Locate every blood parasite and identify its species.
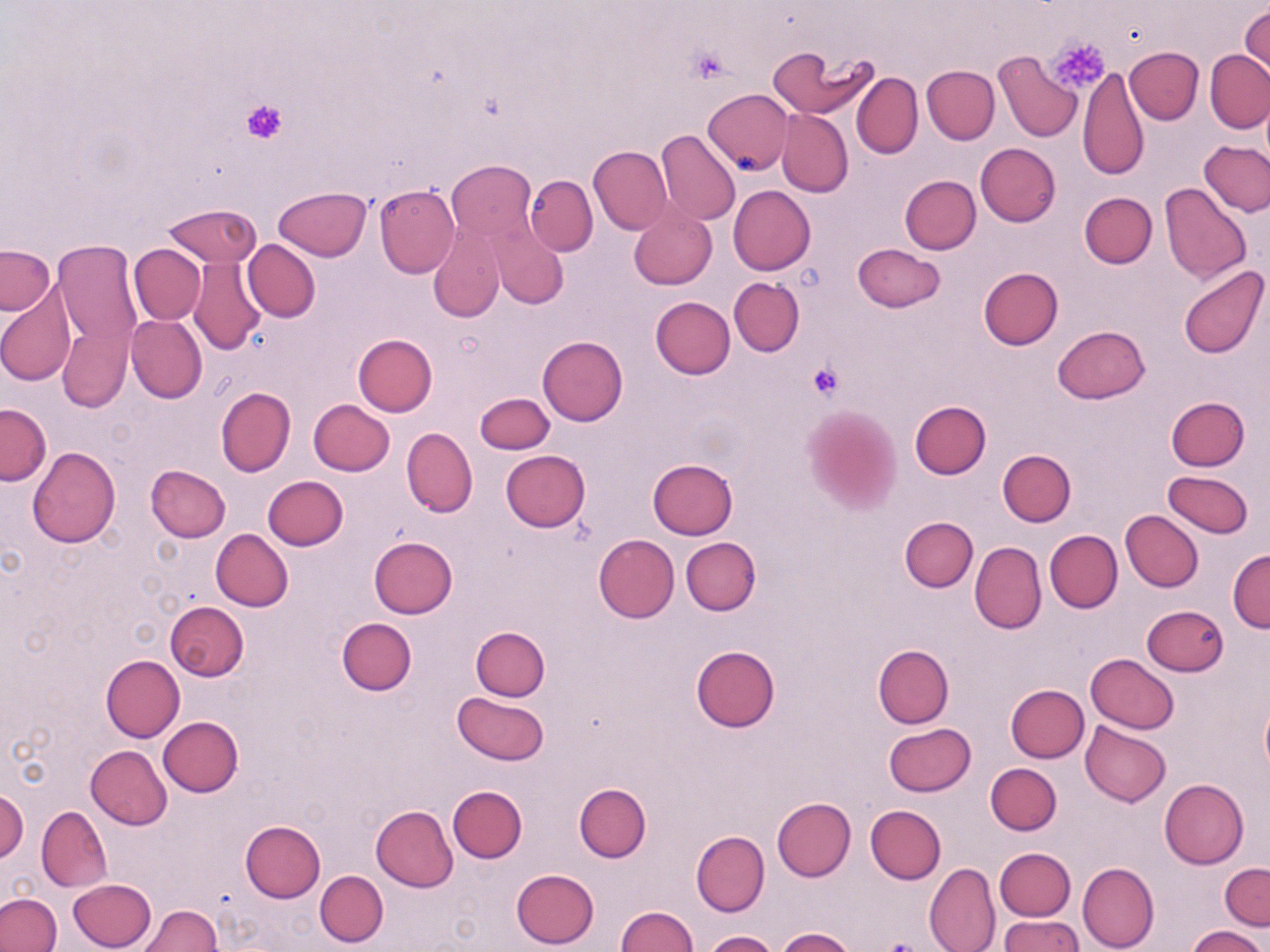

No blood parasites observed.

Approximate bounding boxes as (x1, y1, x2, y2) in pixels. Platelet locations: (1046, 37, 1110, 94), (688, 46, 733, 82), (242, 99, 288, 144), (807, 361, 846, 400), (878, 940, 928, 952). Uninfected red blood cell locations: (1240, 4, 1269, 82), (768, 43, 878, 121), (1125, 47, 1203, 123), (1206, 50, 1270, 134), (994, 51, 1082, 142), (922, 65, 1000, 144), (1078, 67, 1149, 181), (851, 73, 923, 158), (703, 88, 793, 174), (777, 109, 853, 196), (655, 128, 741, 226), (1199, 141, 1270, 215), (976, 143, 1061, 226), (588, 146, 671, 234), (447, 161, 536, 239), (526, 175, 598, 256), (900, 175, 981, 254), (1160, 183, 1251, 285), (374, 184, 459, 278), (274, 185, 372, 260), (728, 186, 815, 274), (1080, 192, 1157, 268), (628, 201, 717, 290), (164, 203, 260, 268), (488, 223, 566, 309), (428, 224, 505, 322), (54, 239, 142, 379), (242, 240, 320, 322), (129, 244, 206, 324), (852, 244, 945, 312), (1, 245, 54, 315), (189, 257, 268, 354), (1177, 264, 1268, 360), (978, 267, 1062, 350), (729, 277, 804, 355), (0, 285, 78, 387), (651, 296, 735, 378), (126, 315, 207, 403), (58, 324, 132, 413), (1051, 325, 1149, 404), (352, 334, 437, 417), (538, 336, 628, 426), (216, 387, 296, 476), (475, 392, 554, 454), (1166, 397, 1249, 471), (309, 399, 395, 476), (909, 401, 990, 479), (0, 403, 50, 484), (801, 407, 900, 513), (401, 429, 477, 517), (26, 447, 120, 547), (997, 449, 1076, 526), (501, 450, 590, 531), (647, 459, 738, 540), (146, 465, 230, 541), (1162, 469, 1254, 538), (263, 476, 348, 550), (1121, 510, 1204, 591), (900, 516, 978, 593), (211, 528, 293, 611), (1045, 530, 1122, 612), (594, 534, 680, 622), (368, 536, 458, 618), (681, 537, 760, 616), (970, 541, 1047, 636), (1228, 549, 1270, 633), (164, 601, 249, 681), (1141, 604, 1230, 677), (336, 619, 416, 695), (471, 626, 551, 700), (873, 644, 953, 728), (690, 646, 779, 732), (1084, 653, 1180, 733), (101, 655, 185, 741), (1005, 685, 1088, 762), (452, 692, 549, 765), (1260, 698, 1270, 777), (158, 717, 243, 797), (1081, 720, 1171, 806), (884, 722, 976, 795), (86, 746, 173, 829), (986, 762, 1061, 835), (1159, 778, 1248, 867), (575, 782, 651, 862), (448, 785, 527, 862), (1, 790, 28, 862), (772, 796, 855, 880), (866, 805, 945, 884), (37, 806, 113, 892), (370, 806, 458, 891), (240, 820, 325, 902), (691, 830, 769, 915), (995, 847, 1076, 921), (930, 854, 1077, 934), (925, 861, 1000, 952), (1077, 861, 1158, 952), (1220, 862, 1270, 931), (510, 869, 600, 949), (315, 870, 388, 946), (69, 879, 156, 951), (0, 893, 61, 952), (135, 905, 221, 952), (617, 906, 698, 952), (999, 914, 1085, 952), (1187, 926, 1264, 952), (775, 927, 855, 952), (705, 930, 778, 951). Slide-level diagnosis: negative for blood parasites. Light microscopy. May-Grünwald-Giemsa-stained preparation. Thin blood film. One field of a larger specimen. 1000x magnification. Image is 1270×952 pixels.